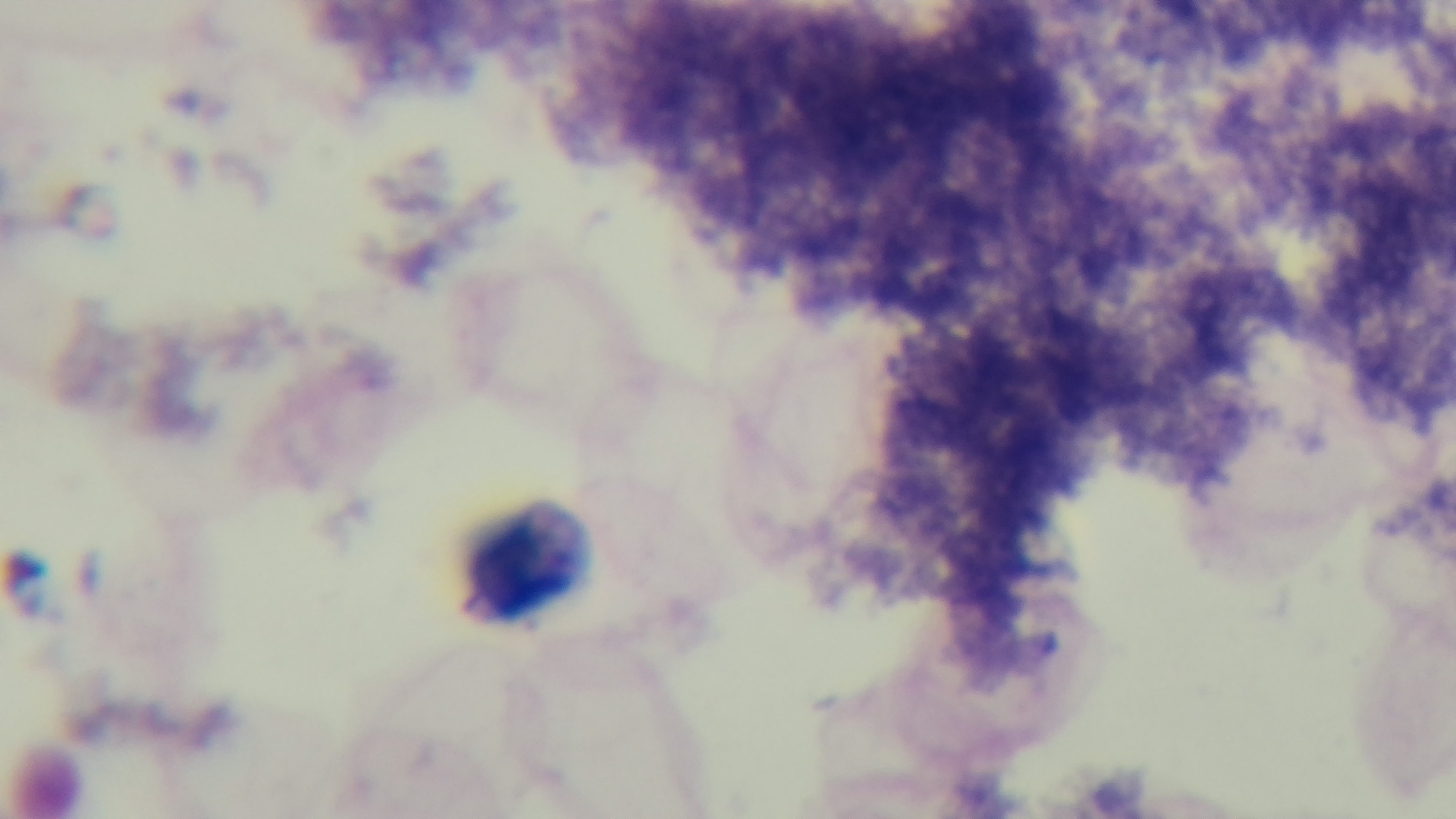
Single field of view. Photomicrograph. Malaria status: negative. Captured with a mounted 4K digital camera. Giemsa stain. Oil-immersion objective, 100x. Preparation: thick.